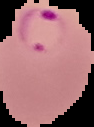
preparation = thin blood film
image type = segmented cell region with the area outside set to black
result = Plasmodium parasites detected
image size = 94×127 pixels